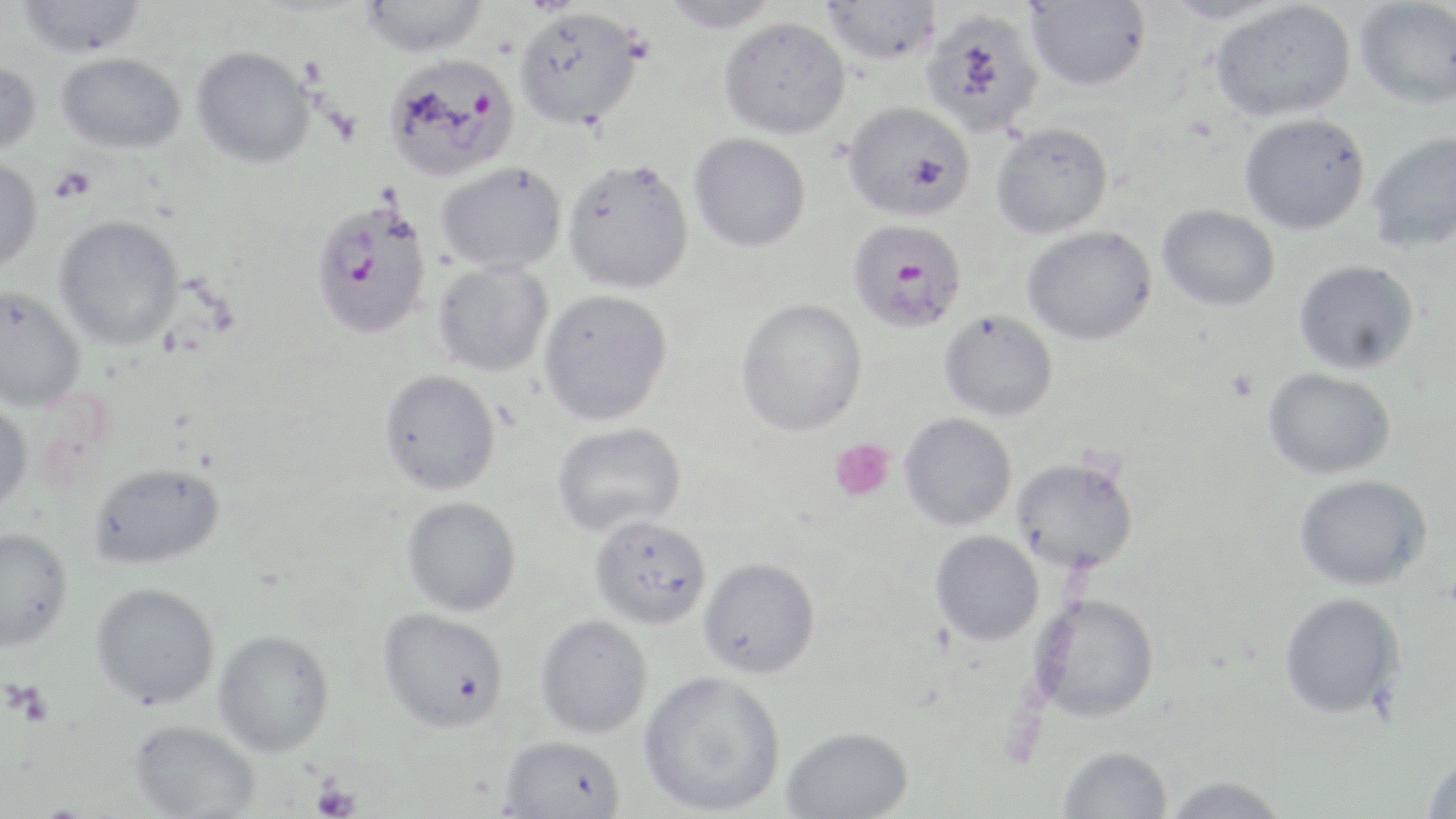
slide-level diagnosis = Plasmodium falciparum
preparation = thin blood film
Plasmodium falciparum-infected red blood cell locations = approximate bounding boxes as (x1, y1, x2, y2) in pixels: (382, 54, 519, 181), (309, 200, 432, 340), (846, 219, 967, 334)
modality = optical microscopy
magnification = 1000x
image size = 1456×819 pixels
uninfected red blood cell locations = approximate bounding boxes as (x1, y1, x2, y2) in pixels: (359, 0, 489, 58), (659, 0, 782, 33), (821, 0, 941, 66), (1159, 0, 1293, 25), (16, 1, 147, 57), (1025, 1, 1151, 91), (1208, 1, 1356, 122), (1354, 1, 1456, 109), (513, 7, 644, 130), (922, 8, 1045, 137), (718, 16, 851, 139), (191, 46, 315, 169), (55, 53, 186, 154), (0, 59, 42, 155), (843, 101, 975, 222), (1240, 113, 1370, 235), (991, 122, 1113, 239), (1367, 131, 1456, 253), (689, 133, 811, 252), (0, 156, 43, 275), (562, 158, 694, 294), (436, 161, 566, 274), (1157, 205, 1279, 311), (54, 215, 184, 350), (1023, 226, 1157, 346), (1294, 260, 1419, 375), (433, 261, 554, 377), (0, 286, 86, 412), (539, 289, 673, 425), (735, 298, 868, 437), (939, 310, 1058, 421), (1263, 368, 1396, 480), (378, 369, 501, 495), (0, 401, 33, 515), (899, 413, 1017, 530), (552, 422, 686, 536), (1011, 456, 1140, 573), (88, 462, 225, 570), (1294, 474, 1432, 591), (401, 496, 521, 617), (589, 516, 711, 630), (0, 527, 73, 653), (930, 531, 1044, 646), (698, 557, 821, 678), (90, 582, 220, 709), (1278, 592, 1404, 720), (1031, 595, 1160, 723), (376, 607, 509, 732), (535, 615, 652, 739), (213, 630, 335, 757), (638, 670, 786, 816), (128, 720, 260, 818), (781, 726, 913, 818), (498, 735, 626, 819), (1057, 746, 1173, 818), (1420, 752, 1456, 819), (1162, 775, 1289, 817)
field of view = single
platelet locations = approximate bounding boxes as (x1, y1, x2, y2) in pixels: (50, 166, 96, 202), (1226, 369, 1260, 403), (829, 438, 895, 503), (8, 682, 53, 727), (312, 780, 361, 819)
stain = May-Grünwald-Giemsa